Name the parasite shown.
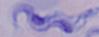

This is a trypanosome.

Photomicrograph. Captured at 1000x magnification.